Comment on the morphology of the red blood cells.
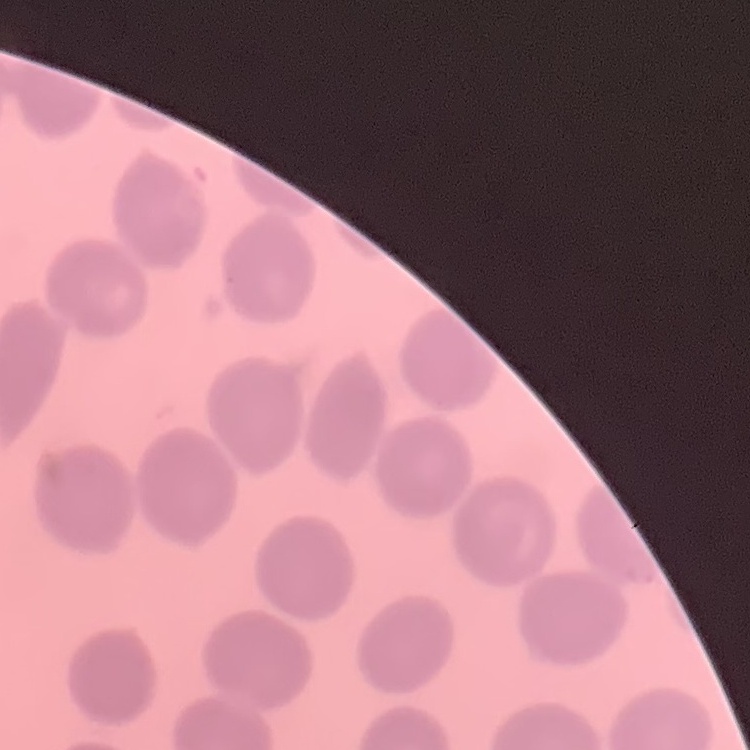

They show no rouleaux formation.

preparation = thin blood smear
stain = Field's or Giemsa
image type = one tile cut from a larger photomicrograph